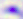
Toxoplasma gondii is shown. 400x magnification. Micrograph.